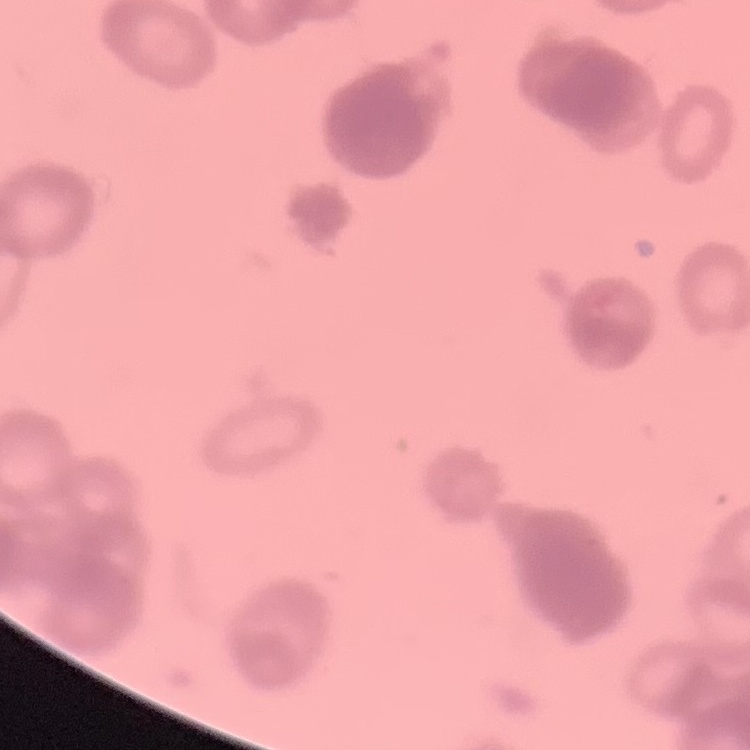

red blood cell morphology = rouleaux formation
preparation = thin peripheral smear
image type = square crop of a larger photomicrograph
stain = Field's or Giemsa